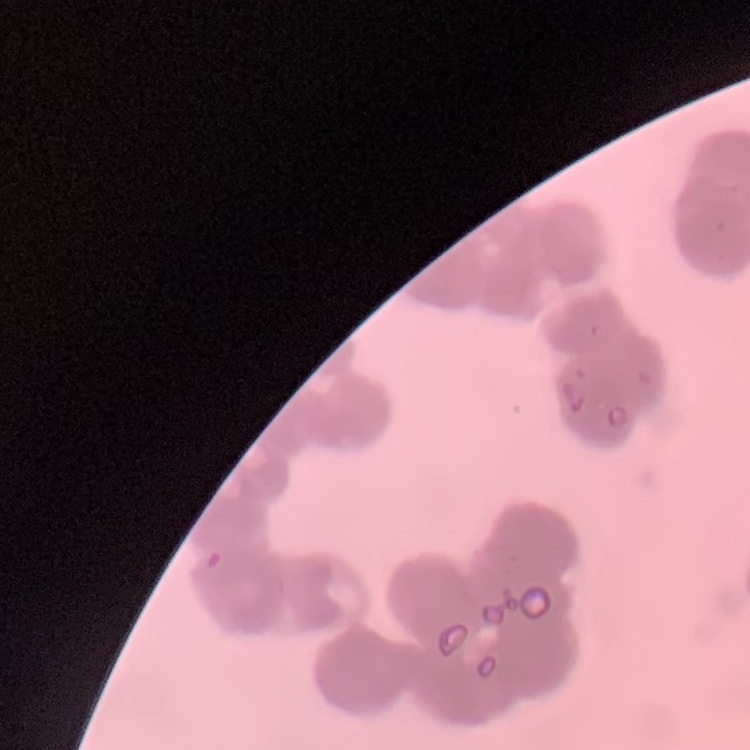
Summary:
  - Erythrocyte morphology: rouleaux formation
  - Stain: Field's or Giemsa
  - Image type: square crop of a larger photomicrograph
  - Preparation: thin blood film